Assess this cell for malaria.
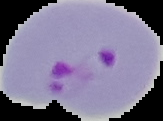
It is parasitized.

preparation = thin blood film
image type = segmented cell region on a black background
image size = 163×121 pixels